Identify the parasite.
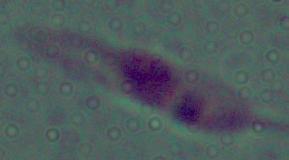

This is Leishmania.

magnification = 1000x
modality = micrograph